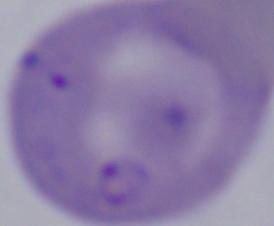

Summary:
  - Modality: photomicrograph
  - Identification: Babesia
  - Magnification: 1000x